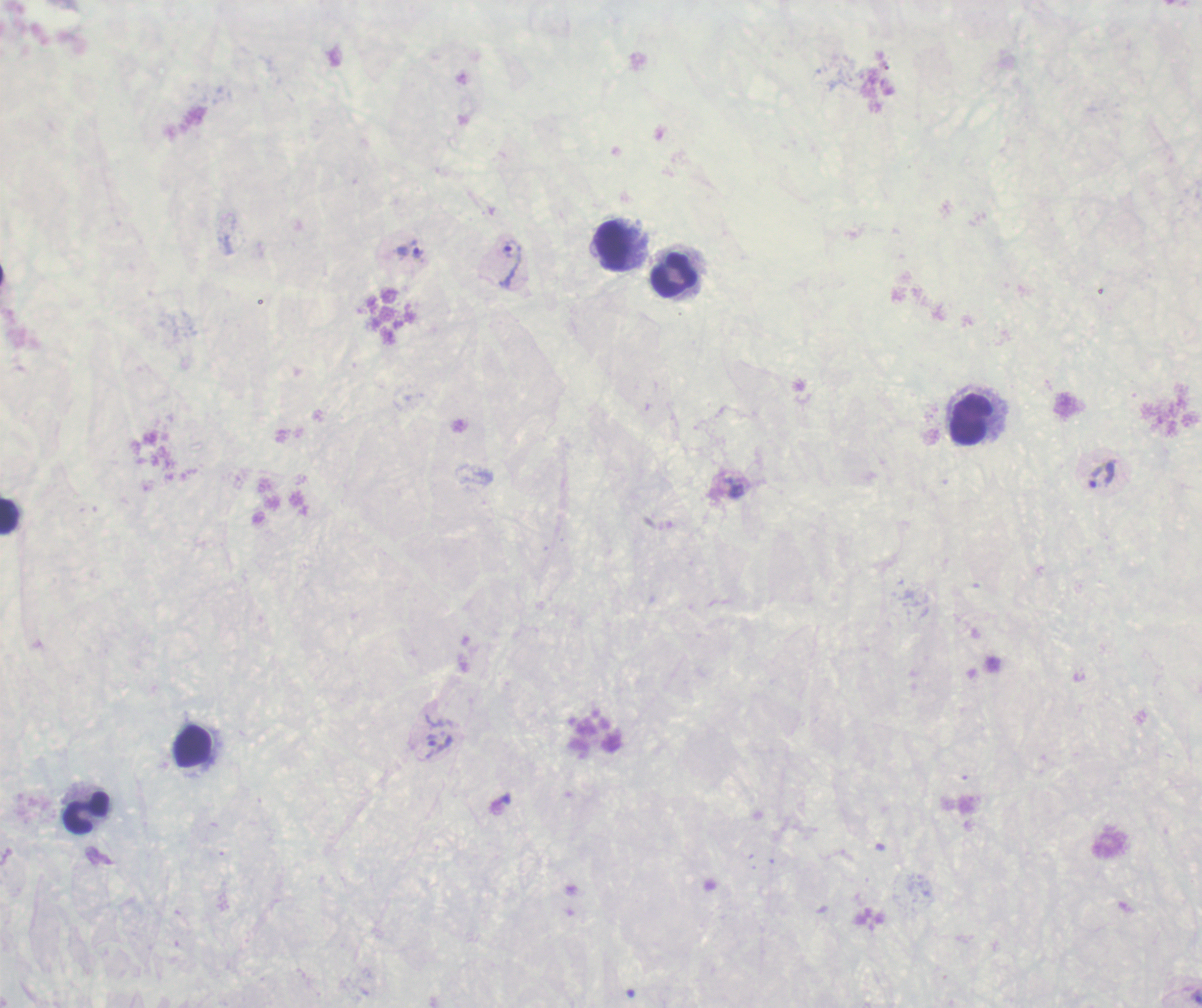

Approximate centers as {x, y} in pixels.
Summary:
  - Trophozoite locations: {410, 251}, {512, 263}, {1101, 474}, {437, 745}
  - Leukocyte locations: {614, 247}, {674, 274}, {971, 419}, {9, 517}, {193, 746}, {85, 813}
  - Image size: 1202×1008 pixels
  - Preparation: thick smear of blood
  - Background quality: poor
  - Result: Plasmodium parasites identified
  - Context: previously used in an actual diagnosis
  - Stain: Romanowsky
  - Magnification: 100x
  - Coloration quality: bad
  - Field of view: one from this slide